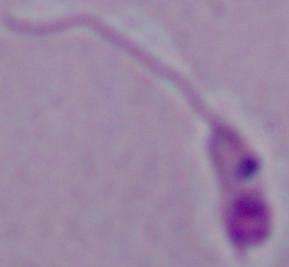
Summary:
  - Magnification: 1000x
  - Modality: photomicrograph
  - Identification: Leishmania